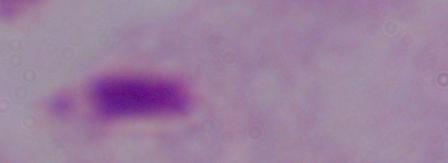
Photomicrograph. A trichomonad is seen. Captured at 1000x magnification.